Assess this cell for malaria.
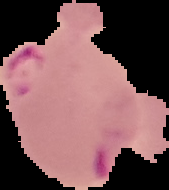

It is parasitized.

{
  "preparation": "thin blood film",
  "image_type": "cell region segmented out of the field of view; surrounding area masked to black",
  "image_size": "169×190 pixels"
}